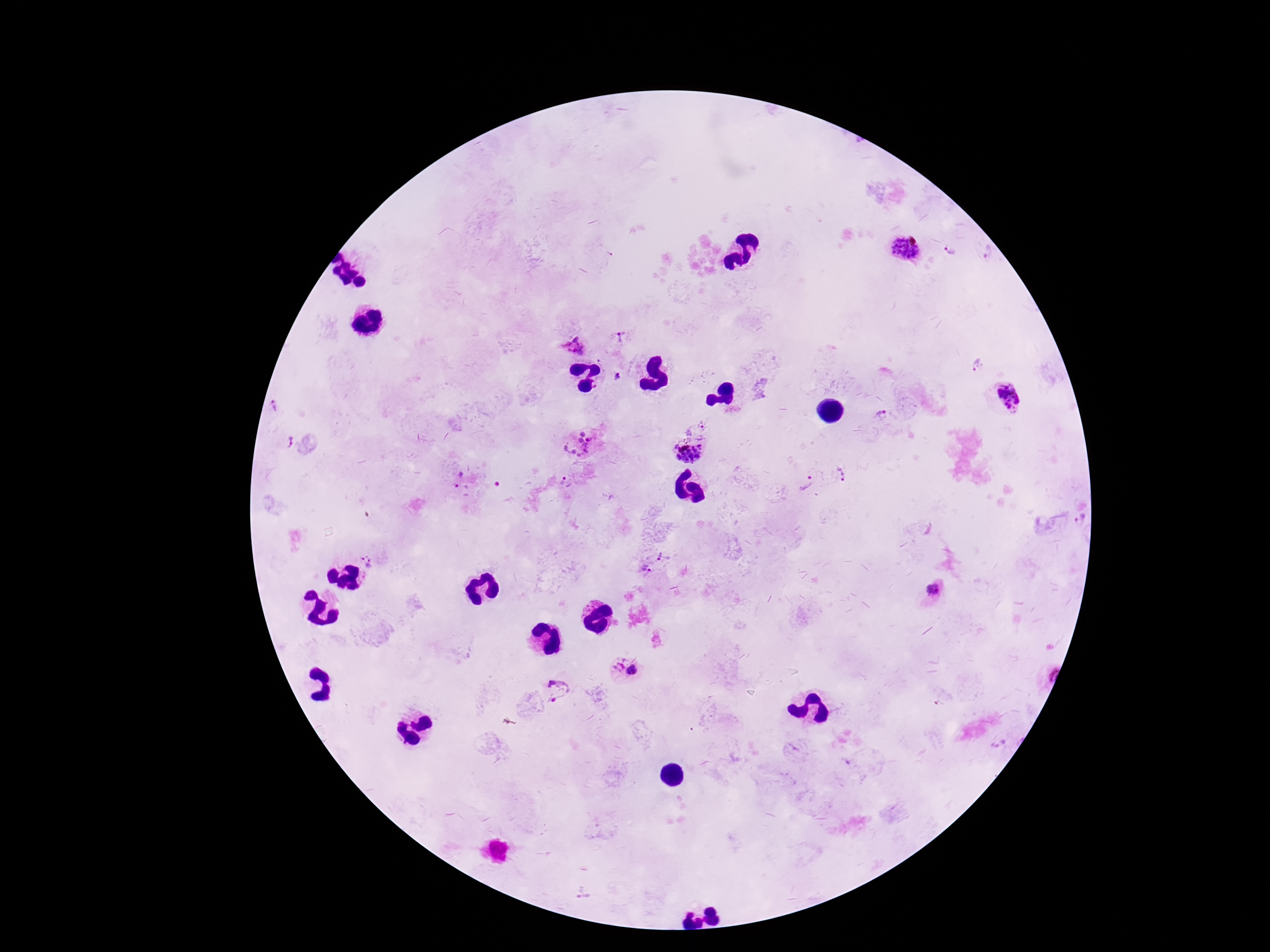

{
  "preparation": "thick blood smear",
  "field_of_view": "single",
  "plasmodium_parasite_locations": "approximate object centers, in pixels from the top-left corner: (x=906, y=247), (x=987, y=250), (x=952, y=251), (x=622, y=337), (x=575, y=345), (x=977, y=364), (x=618, y=377), (x=1010, y=396), (x=273, y=406), (x=882, y=415), (x=699, y=425), (x=285, y=441), (x=578, y=445), (x=690, y=456), (x=841, y=475), (x=457, y=478), (x=567, y=483), (x=806, y=484), (x=498, y=485), (x=1080, y=520), (x=661, y=554), (x=368, y=560), (x=646, y=568), (x=933, y=591), (x=618, y=665), (x=633, y=670), (x=558, y=689)",
  "magnification": "100x",
  "patient_malaria_status": "positive",
  "capture": "smartphone camera through the microscope eyepiece",
  "image_size": "1270×952 pixels",
  "stain": "Giemsa"
}